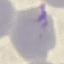

result = no malaria parasites detected
capture = smartphone camera at the microscope eyepiece
stain = Giemsa
image type = cell patch, automatically extracted from a larger field of view and resized to 64 × 64 pixels
preparation = thin blood smear